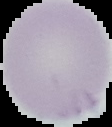 Result: no malaria parasites seen. Cell region segmented out of the field of view; the surrounding area is masked to black. Image is 112×127 pixels. From a thin blood smear.